Comment on the morphology of the erythrocytes.
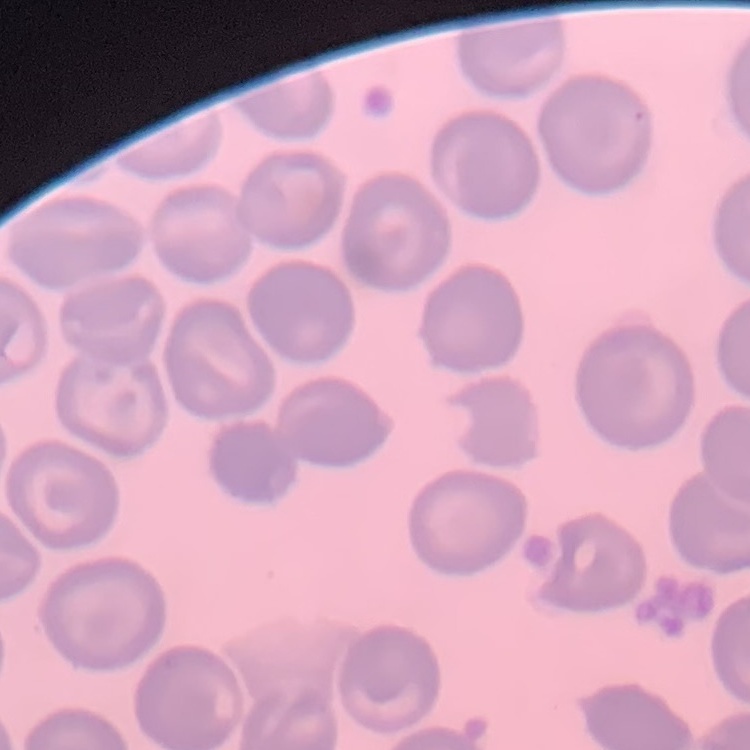

They show no rouleaux formation.

Summary:
  - Stain: Field's or Giemsa
  - Preparation: thin blood smear
  - Image type: one tile cut from a larger photomicrograph